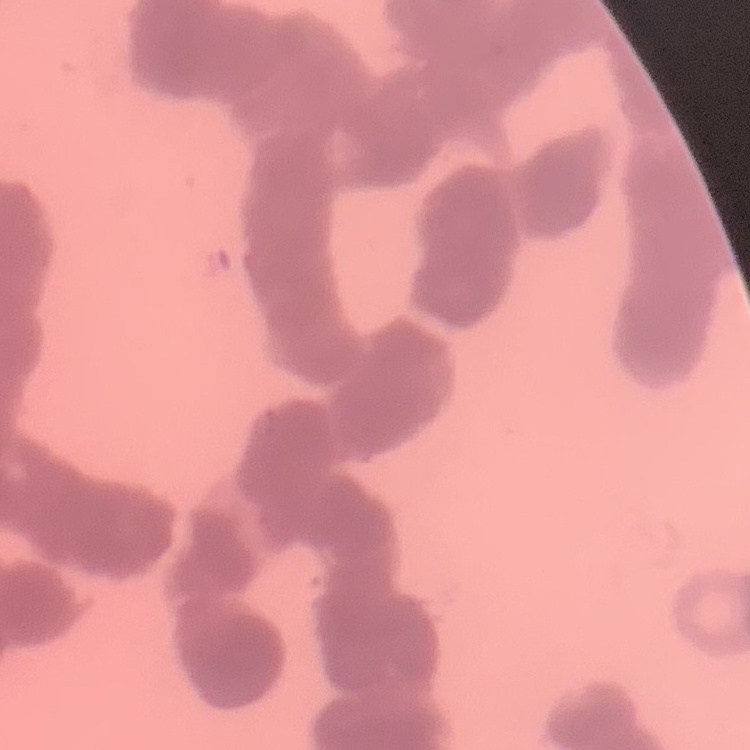

Summary:
  - Red blood cell morphology: rouleaux formation
  - Preparation: thin blood smear
  - Image type: one tile cut from a larger photomicrograph
  - Stain: Field's or Giemsa